Name the blood parasite species.
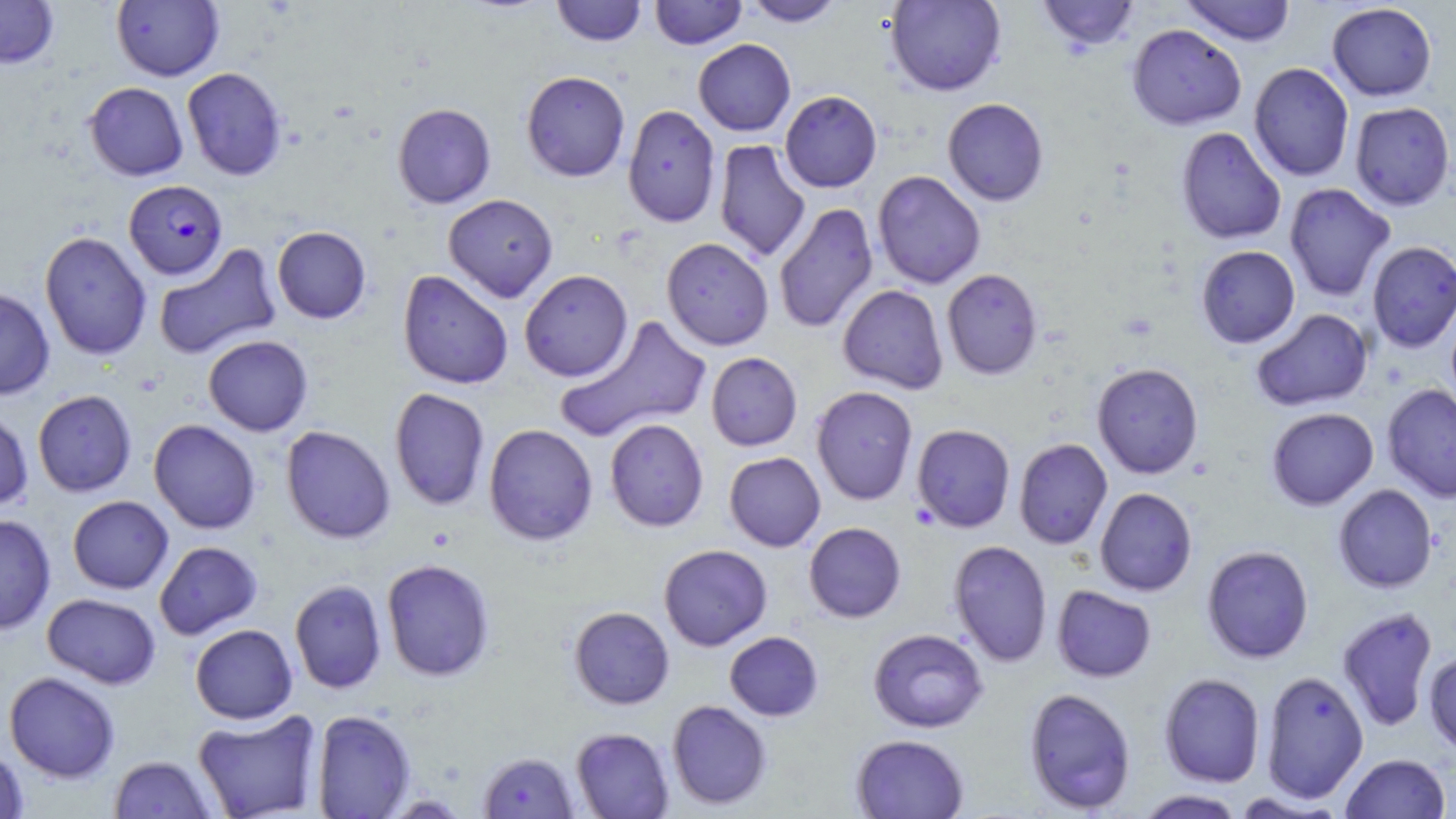

Plasmodium falciparum.

Summary:
  - Coordinate format: approximate bounding boxes as (x1, y1, x2, y2) in pixels
  - Uninfected red blood cell locations: (0, 0, 60, 68), (111, 0, 224, 81), (551, 0, 647, 46), (649, 0, 747, 49), (742, 0, 846, 27), (885, 0, 1006, 96), (1036, 0, 1141, 52), (1180, 0, 1296, 46), (1326, 2, 1437, 101), (1127, 24, 1246, 130), (693, 39, 795, 136), (1248, 62, 1354, 182), (182, 67, 288, 181), (521, 70, 630, 182), (84, 82, 188, 181), (779, 90, 882, 193), (942, 98, 1049, 205), (1349, 102, 1455, 210), (392, 103, 496, 208), (623, 104, 721, 228), (1176, 127, 1286, 245), (714, 139, 811, 262), (872, 170, 986, 289), (1284, 183, 1396, 301), (443, 193, 558, 302), (773, 202, 878, 334), (272, 225, 371, 324), (39, 230, 152, 361), (661, 237, 774, 350), (1367, 241, 1456, 353), (153, 242, 282, 360), (1195, 245, 1300, 348), (942, 268, 1043, 379), (519, 269, 633, 382), (397, 270, 514, 390), (838, 284, 949, 394), (0, 287, 55, 400), (1251, 308, 1373, 411), (556, 315, 712, 442), (203, 335, 313, 436), (706, 352, 802, 451), (1092, 362, 1204, 479), (1381, 383, 1456, 503), (811, 386, 918, 505), (389, 388, 490, 510), (32, 390, 137, 497), (0, 407, 33, 512), (1266, 407, 1378, 510), (605, 418, 708, 532), (148, 419, 261, 534), (483, 423, 598, 546), (911, 424, 1015, 533), (280, 426, 396, 543), (1013, 438, 1112, 550), (724, 451, 826, 551), (1333, 484, 1438, 593), (1095, 488, 1197, 596), (67, 495, 173, 594), (0, 514, 56, 635), (804, 522, 906, 622), (949, 540, 1053, 667), (154, 541, 263, 640), (658, 544, 772, 651), (1201, 545, 1314, 664), (381, 558, 495, 681), (289, 579, 387, 694), (1052, 585, 1156, 682), (42, 593, 161, 689), (569, 606, 674, 709), (1337, 607, 1438, 732), (190, 624, 298, 724), (868, 628, 988, 733), (724, 631, 823, 721), (1423, 650, 1456, 755), (1260, 670, 1369, 803), (4, 671, 121, 783), (1159, 673, 1265, 787), (1024, 687, 1137, 814), (667, 700, 772, 810), (192, 709, 323, 819), (311, 709, 416, 818), (570, 727, 674, 818), (851, 734, 969, 818), (0, 745, 29, 819), (478, 751, 580, 818), (1341, 753, 1451, 819), (109, 756, 217, 818), (1135, 789, 1245, 819), (1229, 791, 1345, 818)
  - Plasmodium falciparum-infected red blood cell locations: (123, 179, 228, 279)
  - Magnification: 1000x
  - Field of view: single
  - Preparation: thin blood film
  - Image size: 1456×819 pixels
  - Stain: May-Grünwald-Giemsa
  - Modality: light microscopy